Report the malaria status.
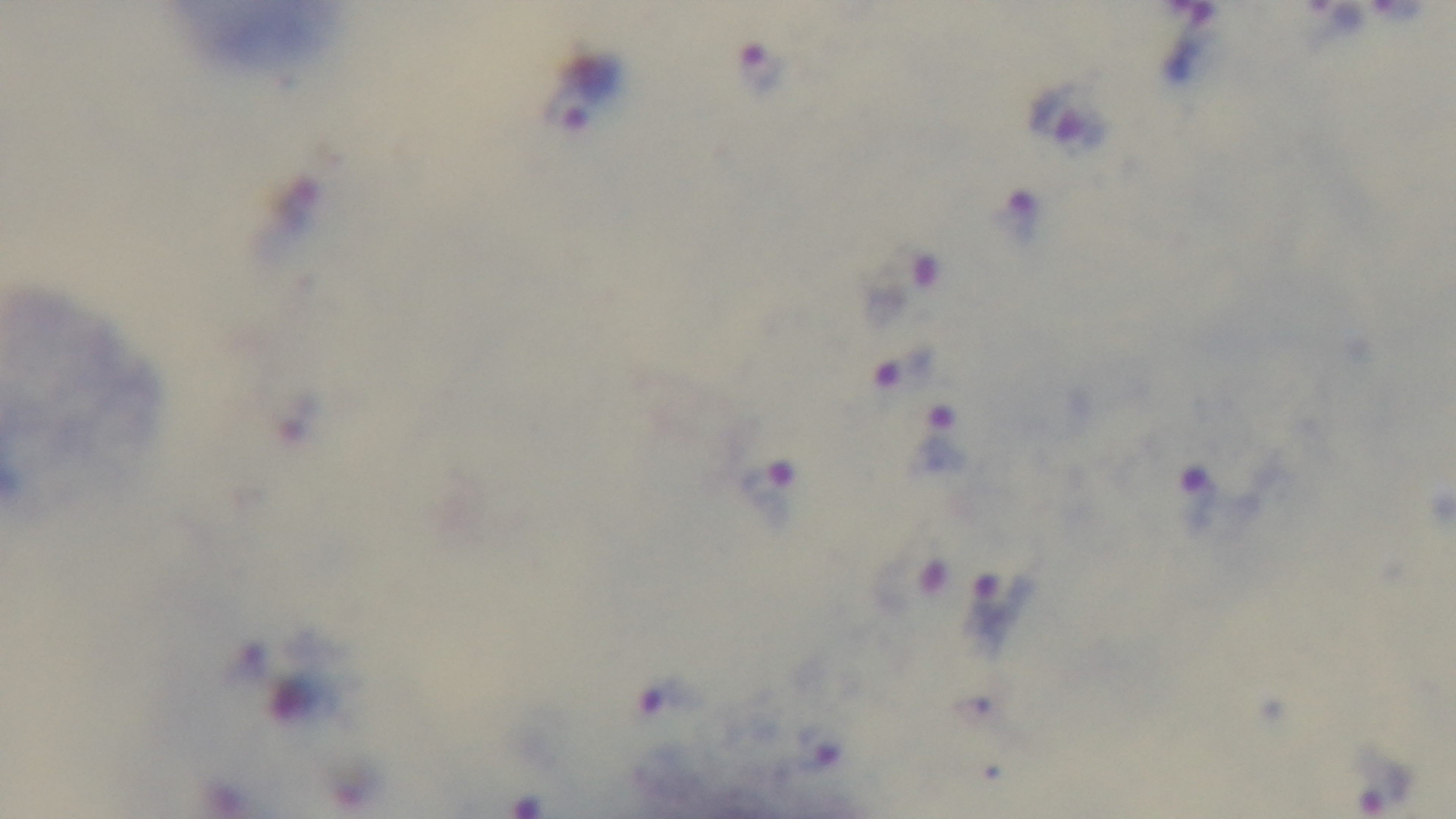

Positive.

Summary:
  - Stain: Giemsa
  - Objective: 100x oil immersion
  - Preparation: thick
  - Field of view: one from the slide
  - Modality: light microscopy
  - Capture: mounted 4K digital camera